Report the malaria status of this cell.
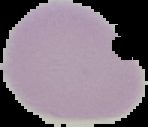

It is uninfected.

Cell region segmented out of the field of view; the surrounding area is masked to black. From a thin blood film. Image is 148×127 pixels.